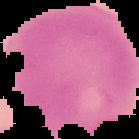 From a thin blood smear. Image is 139×139 pixels. Malaria status: uninfected. Segmented cell region on a black background.